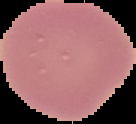

image type = segmented cell region on a black background
preparation = thin blood film
image size = 136×124 pixels
malaria status = uninfected